Identify the parasite.
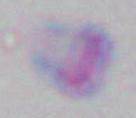
This is Toxoplasma gondii.

Summary:
  - Magnification: 1000x
  - Modality: micrograph